Give the position of every malaria parasite and every leukocyte.
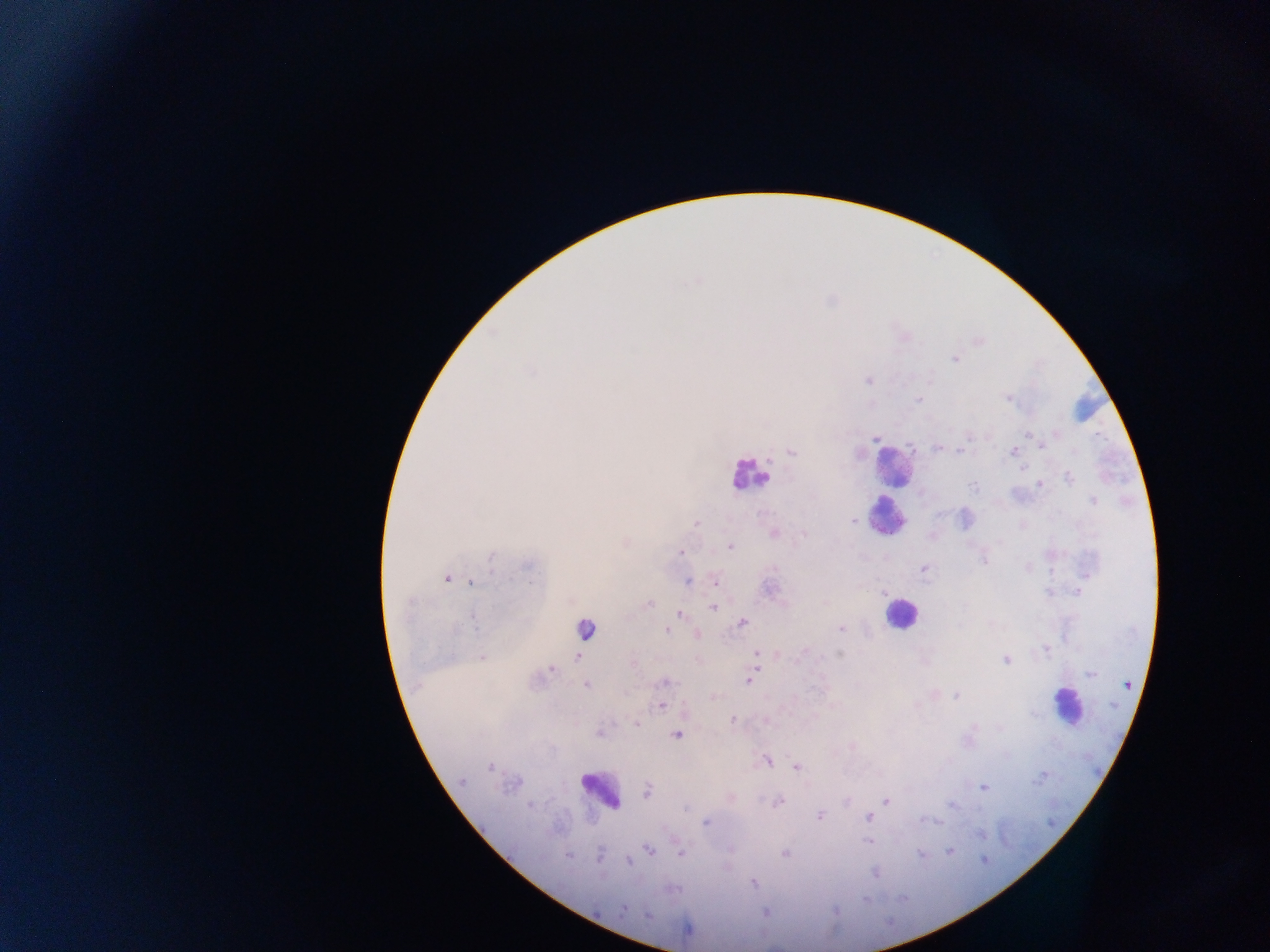
Approximate centers as {x, y} in pixels.
Malaria parasites: {955, 358}, {868, 380}, {1009, 397}, {918, 400}, {874, 437}, {1042, 445}, {937, 448}, {960, 449}, {1013, 451}, {792, 452}, {1069, 478}, {1038, 484}, {974, 486}, {1093, 501}, {852, 519}, {964, 519}, {695, 522}, {774, 533}, {803, 535}, {729, 546}, {680, 552}, {984, 560}, {923, 568}, {446, 578}, {687, 580}, {715, 580}, {472, 582}, {1078, 592}, {648, 603}, {713, 606}, {679, 613}, {743, 623}, {841, 629}, {666, 630}, {695, 634}, {1046, 647}, {756, 653}, {839, 655}, {481, 656}, {576, 656}, {1005, 660}, {551, 668}, {1091, 675}, {750, 680}, {664, 682}, {586, 685}, {956, 694}, {712, 695}, {662, 705}, {732, 720}, {636, 724}, {598, 732}, {677, 734}, {765, 761}, {796, 765}, {489, 767}, {1043, 775}, {461, 781}, {983, 787}, {646, 791}, {778, 801}, {885, 801}, {820, 816}, {868, 817}, {706, 822}, {868, 840}, {649, 850}, {949, 850}, {680, 852}, {785, 853}, {628, 862}, {876, 873}, {752, 882}, {622, 909}, {764, 912}.
Leukocytes: {892, 467}, {749, 474}, {886, 515}, {899, 612}, {585, 631}, {1068, 707}, {599, 790}.

Mobile-phone photograph taken through the microscope. Thick blood smear. Collected in Ghana. One field of view. Image is 1270×952 pixels.